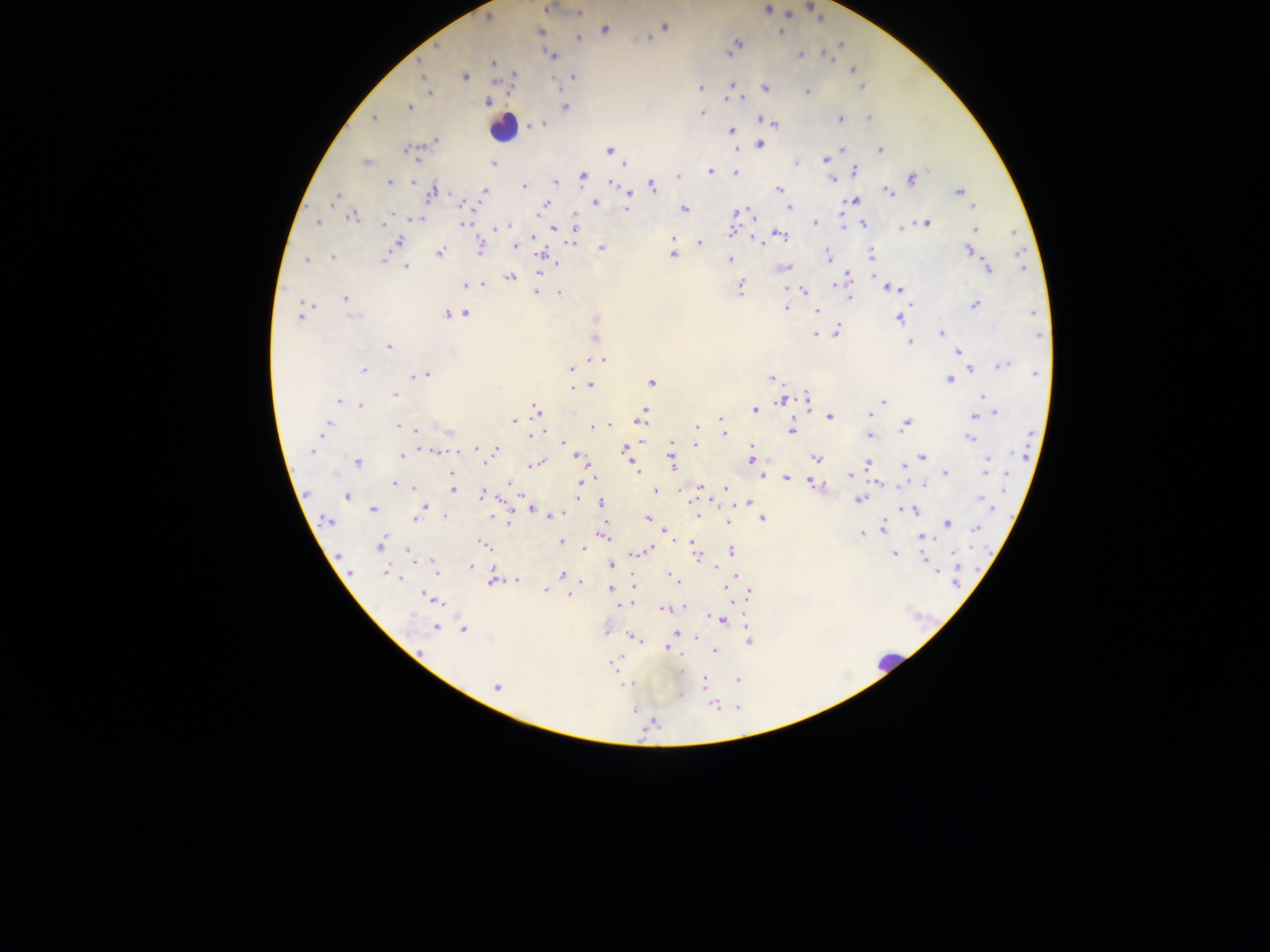
Approximate centers as {x, y} in pixels.
Summary:
  - Leukocyte locations: {502, 127}, {886, 662}
  - Plasmodium parasite locations: {546, 8}, {766, 9}, {578, 13}, {488, 18}, {664, 27}, {604, 30}, {539, 32}, {781, 32}, {647, 37}, {577, 38}, {737, 45}, {839, 45}, {821, 53}, {728, 54}, {552, 55}, {800, 55}, {825, 56}, {419, 61}, {493, 62}, {853, 70}, {422, 75}, {575, 75}, {513, 76}, {464, 77}, {733, 84}, {862, 87}, {764, 88}, {559, 89}, {700, 89}, {805, 91}, {430, 93}, {727, 99}, {742, 99}, {488, 101}, {409, 107}, {565, 107}, {702, 113}, {869, 117}, {374, 118}, {839, 119}, {759, 120}, {772, 122}, {540, 123}, {533, 125}, {731, 131}, {435, 141}, {759, 144}, {735, 147}, {409, 149}, {843, 149}, {880, 150}, {609, 151}, {824, 159}, {416, 161}, {367, 162}, {797, 162}, {493, 164}, {624, 164}, {708, 170}, {854, 170}, {734, 172}, {582, 175}, {678, 176}, {911, 178}, {833, 179}, {390, 182}, {555, 182}, {612, 183}, {524, 186}, {650, 186}, {778, 188}, {433, 191}, {484, 191}, {959, 191}, {888, 192}, {334, 196}, {630, 196}, {854, 200}, {463, 202}, {594, 202}, {544, 204}, {970, 206}, {789, 207}, {626, 209}, {684, 210}, {737, 211}, {751, 211}, {352, 217}, {415, 217}, {317, 221}, {574, 222}, {813, 223}, {863, 223}, {925, 223}, {466, 224}, {844, 225}, {905, 225}, {384, 226}, {510, 226}, {554, 227}, {901, 227}, {502, 228}, {974, 229}, {732, 230}, {1012, 233}, {779, 235}, {533, 236}, {753, 237}, {672, 238}, {398, 241}, {570, 241}, {700, 243}, {479, 246}, {514, 246}, {601, 248}, {969, 249}, {439, 253}, {543, 254}, {672, 254}, {870, 254}, {828, 256}, {332, 258}, {305, 259}, {383, 259}, {730, 260}, {555, 265}, {406, 267}, {784, 267}, {988, 269}, {539, 270}, {847, 274}, {873, 274}, {510, 276}, {483, 283}, {834, 284}, {465, 285}, {740, 286}, {888, 288}, {899, 289}, {536, 291}, {558, 291}, {806, 291}, {345, 297}, {849, 297}, {975, 304}, {786, 308}, {457, 312}, {465, 312}, {301, 313}, {817, 313}, {1033, 313}, {449, 314}, {899, 318}, {595, 319}, {837, 331}, {940, 333}, {814, 334}, {594, 337}, {908, 342}, {388, 347}, {957, 352}, {600, 358}, {1002, 365}, {970, 367}, {570, 369}, {364, 370}, {425, 373}, {772, 377}, {949, 378}, {651, 382}, {590, 385}, {573, 388}, {394, 394}, {806, 397}, {983, 397}, {782, 400}, {338, 401}, {883, 401}, {360, 406}, {756, 410}, {537, 412}, {995, 412}, {643, 414}, {868, 415}, {974, 416}, {720, 417}, {830, 417}, {641, 419}, {513, 421}, {327, 422}, {398, 424}, {905, 424}, {607, 425}, {325, 426}, {592, 426}, {696, 426}, {721, 428}, {417, 430}, {791, 430}, {448, 432}, {538, 434}, {724, 434}, {869, 435}, {970, 438}, {695, 439}, {563, 442}, {672, 442}, {695, 444}, {750, 446}, {494, 449}, {626, 449}, {313, 450}, {436, 451}, {458, 451}, {752, 453}, {400, 456}, {577, 456}, {923, 457}, {816, 459}, {987, 459}, {356, 461}, {483, 461}, {672, 461}, {752, 462}, {868, 463}, {536, 464}, {904, 467}, {587, 468}, {635, 469}, {985, 470}, {945, 473}, {762, 474}, {850, 475}, {786, 478}, {582, 479}, {811, 482}, {393, 483}, {880, 483}, {510, 484}, {923, 484}, {413, 487}, {701, 487}, {725, 488}, {452, 490}, {654, 491}, {482, 494}, {577, 495}, {346, 496}, {980, 497}, {859, 499}, {691, 501}, {600, 502}, {748, 503}, {424, 505}, {372, 509}, {532, 509}, {915, 509}, {902, 510}, {422, 511}, {554, 515}, {444, 516}, {549, 516}, {416, 518}, {645, 518}, {695, 518}, {762, 518}, {492, 519}, {508, 521}, {727, 521}, {326, 522}, {946, 523}, {976, 527}, {882, 528}, {664, 532}, {862, 533}, {601, 536}, {921, 537}, {561, 541}, {693, 543}, {380, 545}, {484, 545}, {583, 549}, {648, 549}, {694, 550}, {409, 551}, {636, 552}, {731, 552}, {894, 553}, {697, 554}, {924, 558}, {433, 560}, {611, 565}, {471, 567}, {715, 568}, {958, 570}, {435, 571}, {349, 573}, {386, 573}, {562, 574}, {398, 576}, {631, 578}, {491, 579}, {516, 579}, {674, 580}, {730, 580}, {582, 583}, {610, 588}, {727, 590}, {544, 591}, {749, 593}, {569, 594}, {429, 597}, {618, 604}, {682, 607}, {663, 608}, {721, 620}, {436, 626}, {464, 630}, {606, 631}, {677, 633}, {695, 636}, {631, 637}, {748, 640}, {667, 648}, {714, 651}, {613, 664}, {737, 679}, {702, 683}, {497, 685}, {626, 685}
  - Preparation: thick blood film
  - Field of view: single
  - Image size: 1270×952 pixels
  - Capture: mobile-phone photograph through a microscope
  - Country: Ghana